Assess this cell for malaria.
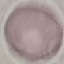
Uninfected.

capture = smartphone through the microscope eyepiece
image type = automatically extracted cell patch, resized to 64 × 64 pixels
preparation = thin blood smear
stain = Giemsa